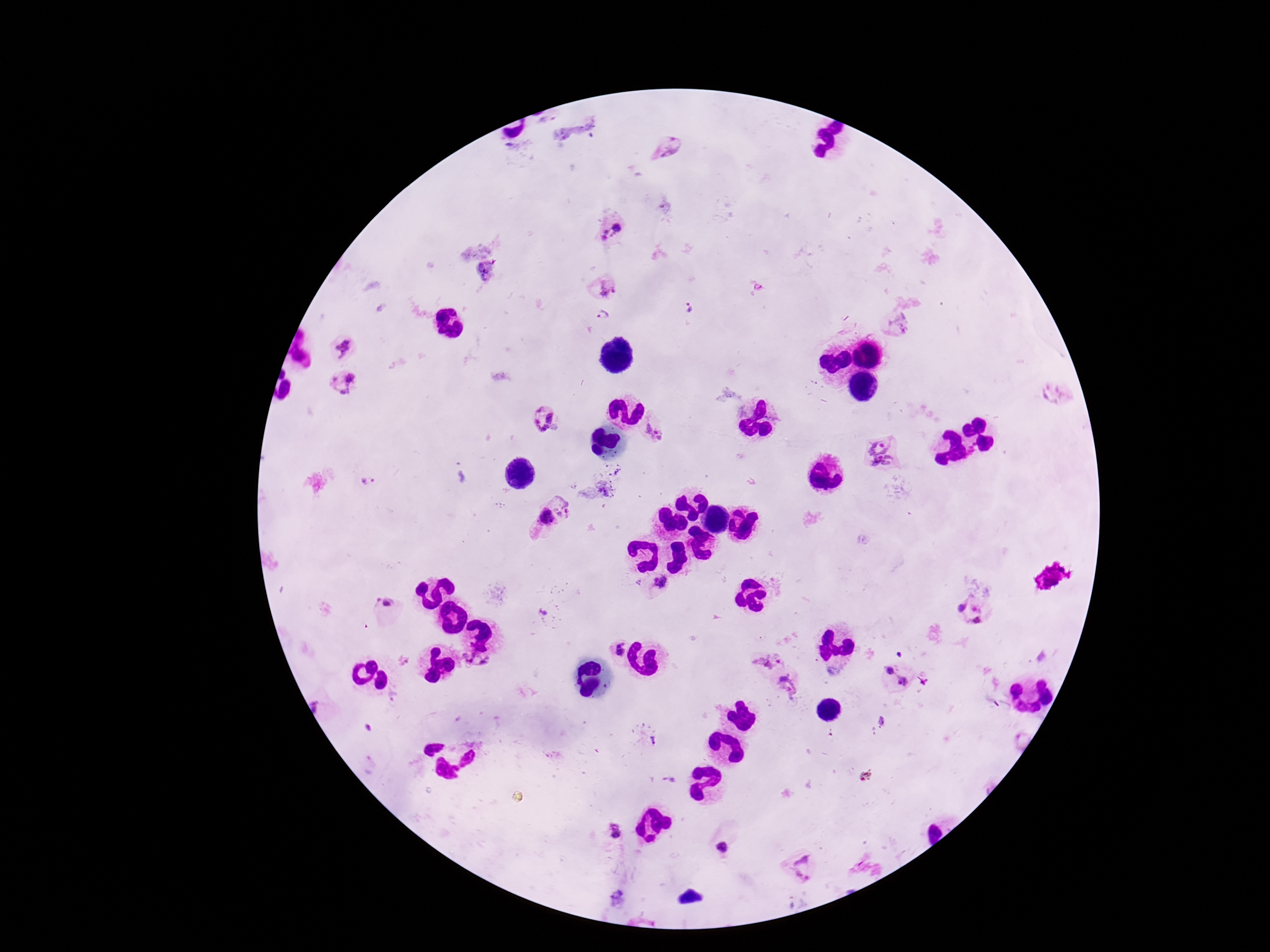

Approximate centers as (x, y) in pixels. Plasmodium parasite locations: (668, 147), (613, 228), (486, 271), (605, 287), (686, 310), (603, 317), (896, 324), (342, 348), (344, 382), (1052, 395), (544, 418), (655, 433), (881, 450), (367, 480), (560, 502), (545, 518), (661, 585), (385, 604), (958, 606), (974, 607), (978, 620), (616, 649), (767, 660), (478, 665), (887, 671), (905, 681), (788, 684), (653, 741), (612, 830), (723, 849), (803, 870). Giemsa stain. Single field of view. Image is 1270×952 pixels. Photographed through the microscope eyepiece with a smartphone camera. Thick peripheral-blood smear. 100x magnification. Patient malaria status: positive.